Point out each malaria parasite.
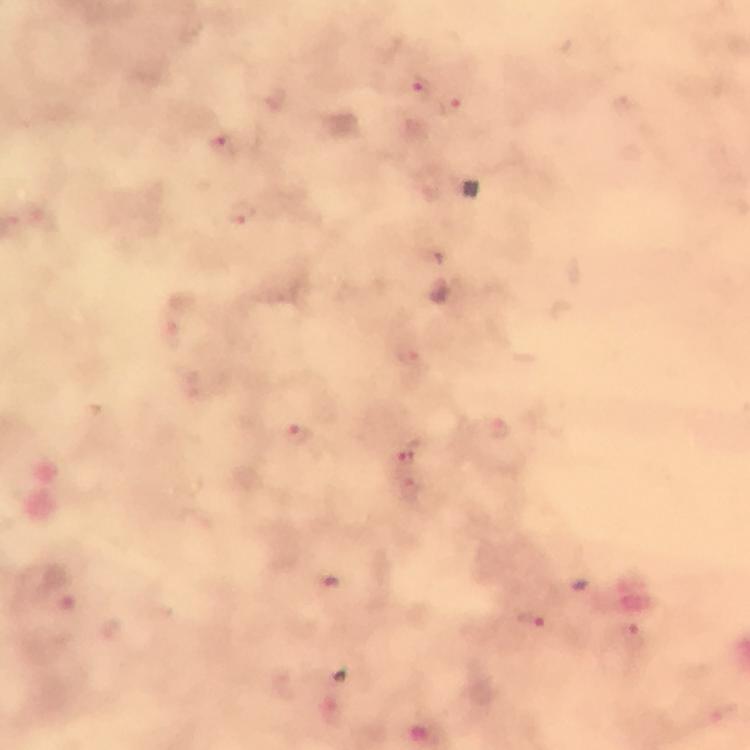
Approximate centers as [x, y] in pixels.
Malaria parasites: [421, 85], [453, 107], [224, 144], [242, 211], [411, 357], [501, 434], [297, 435], [410, 453], [532, 622], [633, 636].

From a diagnostic examination for malaria. Image is 750×750 pixels. Thick blood film. 100x magnification. Giemsa stain. A crop from one field of view. Photographed with a smartphone mounted on the microscope. Immersion oil applied.